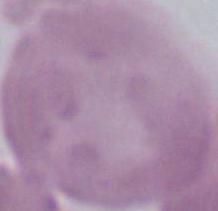
Summary:
  - Magnification: 1000x
  - Modality: micrograph
  - Identification: red blood cell